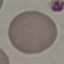
result = no malaria parasites seen
preparation = thin smear
image type = automatically extracted cell patch, resized to 64 × 64 pixels
stain = Giemsa
capture = smartphone through the microscope eyepiece